Locate every cell, classifying each as a parasitized red blood cell, an uninfected red blood cell, or a white blood cell.
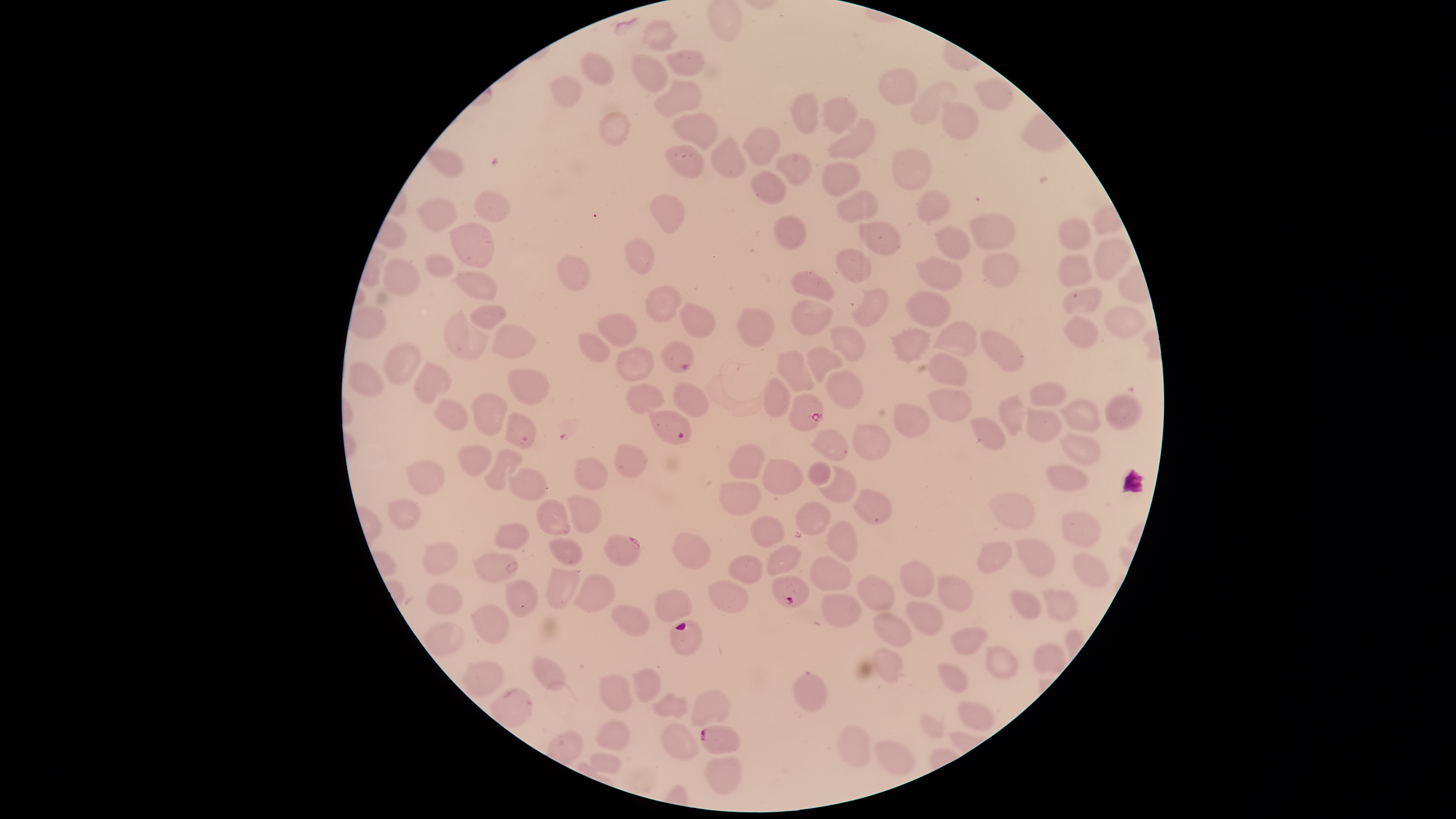
Approximate bounding boxes as [left, top, right, bottom] in pixels.
Parasitized red blood cells: [661, 341, 694, 374], [787, 392, 825, 432], [647, 411, 691, 445], [505, 412, 536, 449], [603, 534, 641, 567], [772, 575, 810, 609], [700, 725, 740, 755].
Uninfected red blood cells: [641, 18, 679, 52], [666, 48, 704, 77], [581, 50, 615, 88], [631, 53, 669, 95], [877, 67, 918, 104], [549, 72, 585, 109], [974, 78, 1016, 111], [651, 79, 704, 118], [909, 81, 957, 126], [789, 92, 818, 134], [822, 95, 859, 134], [941, 101, 980, 140], [597, 111, 631, 147], [671, 112, 719, 151], [826, 118, 876, 160], [742, 127, 782, 166], [709, 134, 747, 178], [664, 143, 706, 178], [425, 148, 465, 178], [891, 149, 930, 191], [775, 152, 812, 186], [819, 161, 860, 198], [750, 169, 788, 205], [475, 189, 511, 223], [836, 189, 878, 223], [916, 189, 952, 223], [649, 193, 686, 233], [416, 196, 459, 231], [969, 212, 1015, 250], [773, 214, 807, 250], [1056, 217, 1091, 250], [449, 221, 494, 269], [859, 221, 902, 256], [934, 225, 971, 261], [1092, 236, 1133, 281], [624, 237, 654, 275], [834, 247, 871, 285], [424, 252, 455, 278], [982, 253, 1021, 288], [1057, 253, 1094, 287], [556, 254, 592, 292], [915, 256, 963, 292], [380, 257, 420, 296], [790, 269, 835, 303], [454, 271, 496, 301], [645, 284, 682, 324], [850, 287, 891, 328], [1062, 287, 1103, 317], [904, 289, 953, 327], [791, 299, 833, 338], [678, 301, 717, 338], [1103, 302, 1150, 339], [468, 304, 507, 331], [349, 305, 387, 339], [735, 307, 777, 347], [442, 309, 491, 360], [597, 311, 638, 348], [1062, 314, 1101, 348], [931, 320, 978, 358], [492, 323, 538, 359], [828, 325, 866, 362], [887, 327, 932, 365], [979, 328, 1025, 373], [577, 332, 611, 362], [383, 342, 421, 385], [615, 345, 654, 382], [805, 345, 845, 383], [776, 349, 816, 392], [926, 353, 968, 387], [348, 360, 386, 397], [413, 360, 451, 405], [507, 367, 550, 406], [824, 368, 863, 410], [762, 377, 790, 418], [1028, 380, 1067, 407], [672, 382, 711, 418], [625, 383, 665, 415], [928, 388, 974, 423], [470, 392, 507, 436], [996, 393, 1025, 438], [1104, 394, 1143, 430], [432, 397, 470, 432], [1055, 398, 1102, 433], [891, 402, 932, 439], [1025, 406, 1063, 443], [969, 417, 1008, 452], [852, 423, 891, 462], [808, 427, 850, 462], [1059, 433, 1101, 467], [727, 443, 766, 479], [614, 444, 648, 477], [456, 445, 493, 477], [483, 448, 522, 491], [574, 457, 608, 491], [762, 457, 805, 497], [404, 459, 445, 496], [808, 461, 834, 486], [1045, 463, 1089, 494], [816, 465, 857, 503], [508, 467, 548, 502], [718, 481, 761, 516], [853, 489, 893, 525], [987, 492, 1035, 532], [567, 495, 603, 534], [388, 497, 420, 529], [535, 498, 571, 536], [793, 501, 831, 536], [1059, 510, 1103, 549], [750, 515, 785, 550], [824, 520, 858, 562], [494, 522, 531, 550], [673, 531, 712, 572], [548, 537, 584, 568], [1015, 537, 1056, 579], [975, 540, 1012, 576], [421, 542, 460, 576], [766, 544, 801, 577], [1071, 550, 1110, 590], [471, 551, 519, 584], [728, 553, 763, 585], [809, 555, 852, 592], [900, 560, 934, 598], [544, 567, 582, 609], [571, 573, 615, 613], [856, 573, 896, 610], [936, 574, 972, 612], [504, 578, 539, 617], [708, 580, 750, 613], [425, 581, 464, 614], [1041, 588, 1079, 622], [654, 589, 692, 622], [1009, 589, 1042, 621], [821, 592, 863, 627], [906, 600, 943, 637], [471, 603, 512, 645], [610, 604, 650, 636], [872, 613, 913, 649], [421, 622, 464, 655], [949, 626, 989, 656], [1032, 642, 1066, 674], [984, 645, 1019, 680], [873, 646, 906, 684], [532, 655, 566, 691], [461, 660, 506, 699], [936, 662, 969, 694], [630, 666, 662, 703], [791, 669, 828, 714], [599, 673, 633, 712], [490, 687, 533, 728], [690, 689, 733, 726], [650, 692, 691, 720], [957, 700, 995, 730], [919, 712, 945, 738], [595, 718, 632, 751], [659, 722, 700, 761], [836, 724, 871, 768], [872, 738, 915, 777], [589, 753, 623, 776], [704, 756, 741, 795].
No white blood cells identified.

capture: smartphone photograph through the microscope eyepiece
species: Plasmodium falciparum
stain: Giemsa
image_size: 1456×819 pixels
preparation: thin blood film
visible_region: circular
field_of_view: single